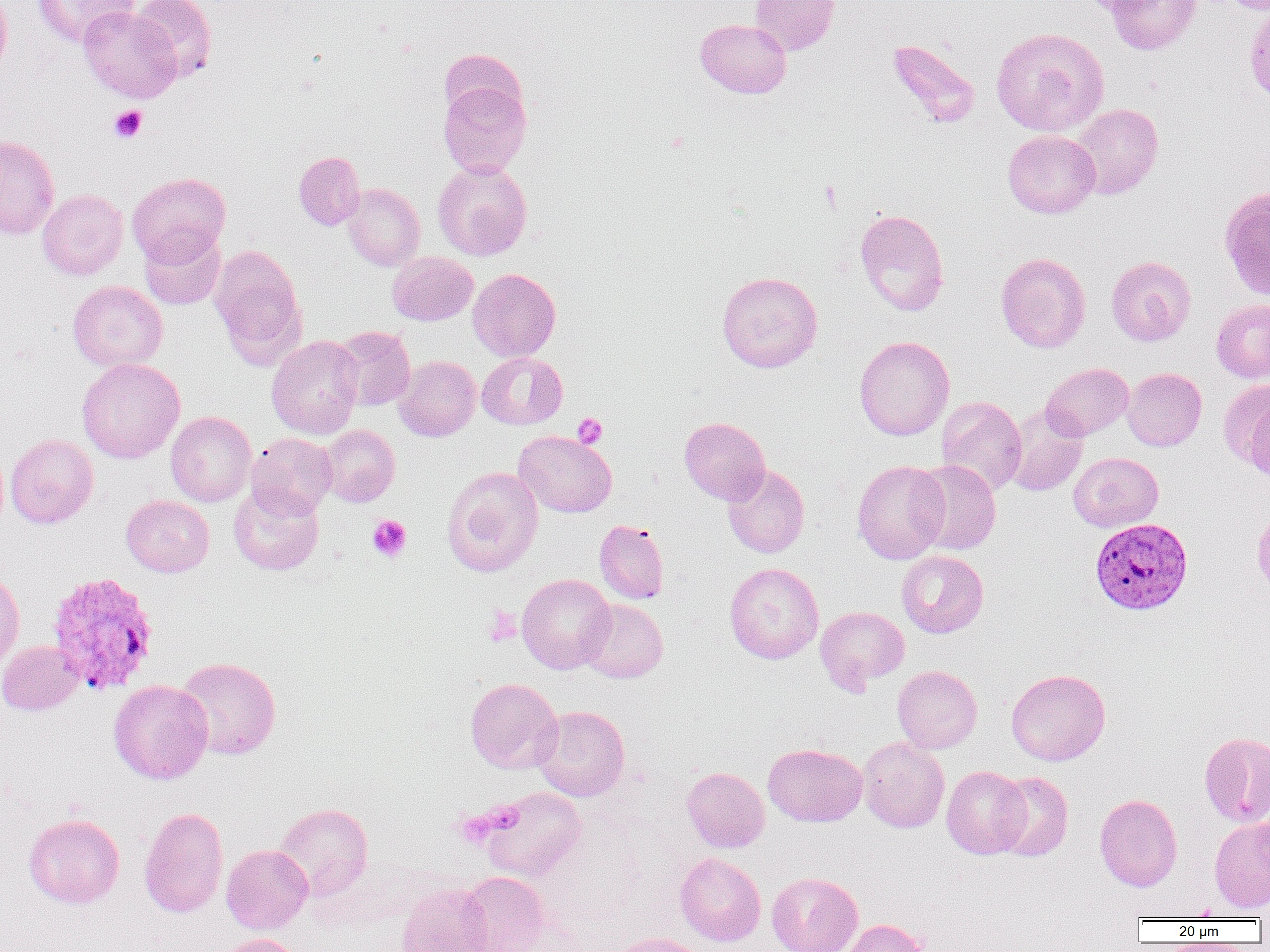

slide-level diagnosis = Plasmodium vivax
uninfected red blood cell locations = approximate bounding boxes as (x1, y1, x2, y2) in pixels: (0, 0, 11, 80), (32, 0, 138, 48), (130, 0, 217, 82), (750, 0, 839, 55), (1076, 0, 1165, 16), (1106, 0, 1201, 55), (1244, 2, 1270, 105), (78, 5, 181, 103), (695, 18, 791, 98), (991, 26, 1110, 136), (887, 38, 982, 128), (438, 48, 529, 125), (438, 78, 532, 178), (1069, 103, 1163, 199), (1003, 130, 1100, 218), (0, 135, 60, 239), (293, 151, 364, 230), (432, 160, 532, 261), (127, 172, 230, 265), (342, 183, 425, 271), (1219, 186, 1270, 300), (37, 189, 128, 280), (854, 209, 949, 316), (139, 227, 226, 310), (209, 244, 305, 364), (387, 252, 478, 326), (995, 252, 1091, 353), (1106, 256, 1196, 346), (468, 268, 560, 362), (717, 271, 822, 372), (68, 280, 168, 372), (1211, 299, 1270, 382), (331, 326, 415, 411), (266, 335, 364, 439), (854, 335, 954, 440), (476, 352, 567, 429), (394, 356, 480, 441), (76, 358, 185, 464), (1041, 363, 1134, 440), (1122, 368, 1207, 451), (1220, 381, 1270, 471), (936, 396, 1027, 494), (1243, 397, 1270, 485), (1004, 404, 1088, 496), (166, 411, 256, 506), (679, 416, 770, 504), (319, 425, 400, 506), (514, 430, 617, 517), (246, 432, 337, 519), (5, 434, 98, 529), (1068, 452, 1163, 532), (852, 460, 950, 564), (911, 460, 1001, 555), (722, 464, 810, 558), (442, 466, 544, 577), (228, 484, 324, 575), (121, 495, 214, 577), (1252, 505, 1269, 599), (594, 519, 668, 604), (897, 550, 989, 638), (724, 562, 824, 663), (0, 570, 25, 672), (516, 573, 615, 674), (579, 598, 667, 683), (815, 606, 910, 693), (0, 641, 83, 715), (176, 656, 281, 759), (892, 665, 982, 753), (1006, 669, 1110, 765), (465, 678, 563, 774), (108, 679, 213, 784), (533, 705, 630, 802), (1199, 731, 1270, 827), (857, 736, 950, 833), (763, 743, 867, 826), (681, 766, 770, 853), (942, 766, 1030, 859), (992, 771, 1073, 862), (480, 787, 586, 883), (1095, 793, 1182, 891), (274, 802, 373, 900), (139, 806, 229, 918), (23, 813, 124, 909), (1209, 816, 1270, 913), (221, 844, 313, 934), (675, 852, 766, 946), (458, 871, 550, 952), (767, 872, 863, 952), (396, 881, 493, 952), (838, 919, 930, 952), (607, 932, 713, 952), (209, 933, 305, 952)
Plasmodium vivax-infected red blood cell locations = approximate bounding boxes as (x1, y1, x2, y2) in pixels: (1093, 521, 1196, 618), (45, 571, 159, 695)
magnification = 1000x
field of view = single
image size = 1270×952 pixels
modality = optical microscopy
preparation = thin blood smear
platelet locations = approximate bounding boxes as (x1, y1, x2, y2) in pixels: (109, 105, 147, 142), (820, 181, 842, 211), (573, 413, 607, 448), (367, 515, 412, 561), (483, 606, 521, 646), (453, 810, 498, 848)